Classify this cell by malaria status.
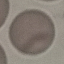
It is uninfected.

Cell patch, automatically extracted from a larger field of view and resized to 64 × 64 pixels. Acquired by smartphone through the microscope eyepiece. Thin smear of blood. Giemsa stain.